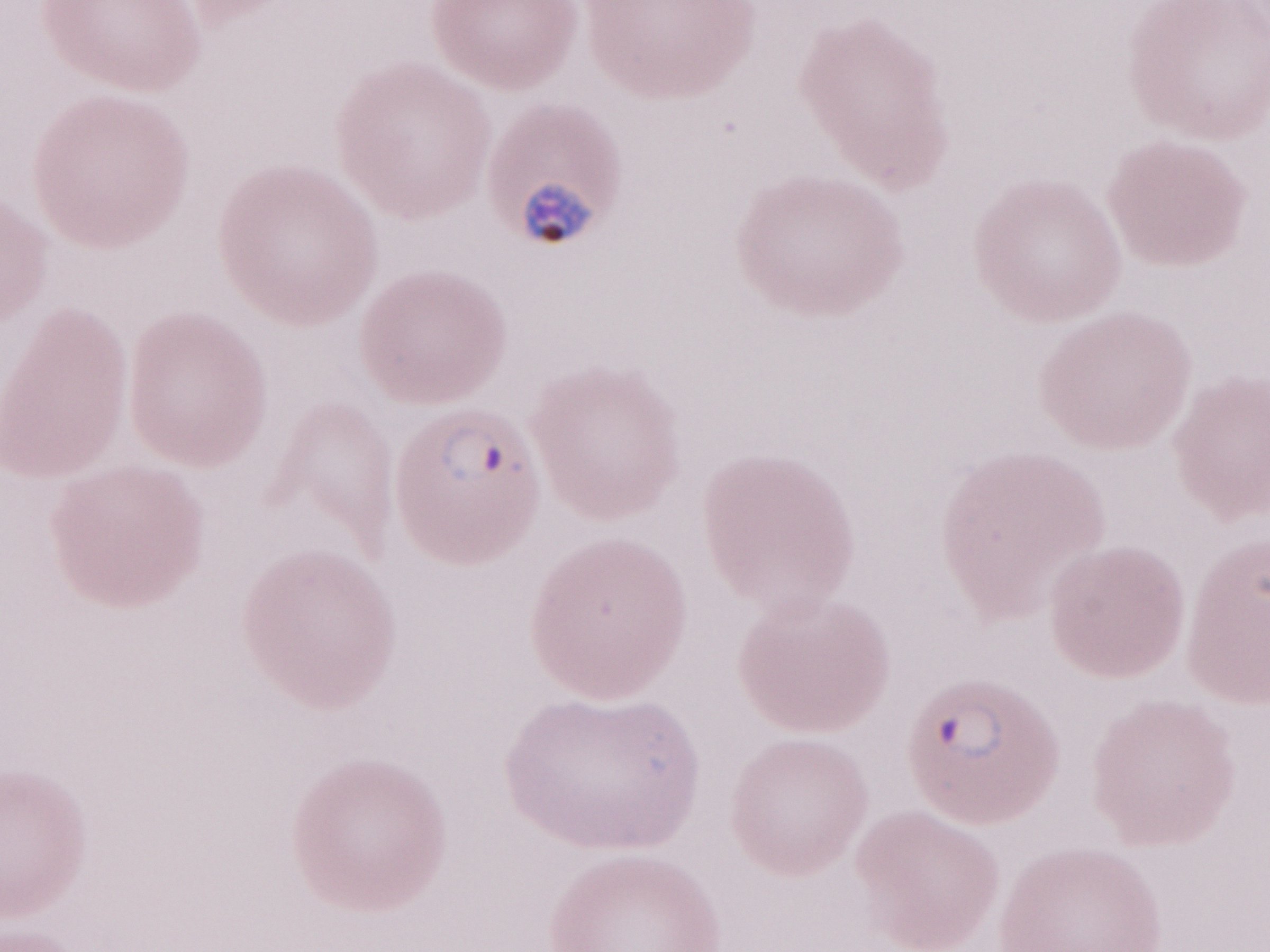
Magnification: 1,000x. May-Grünwald-Giemsa stain. Image is 1270×952 pixels. Olympus BX43 microscope and DP73 digital camera. Thin blood smear. Patient diagnosis: malaria infection. One field of this slide.